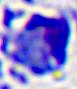

Summary:
  - Identification: leukocyte
  - Modality: micrograph
  - Magnification: 400x